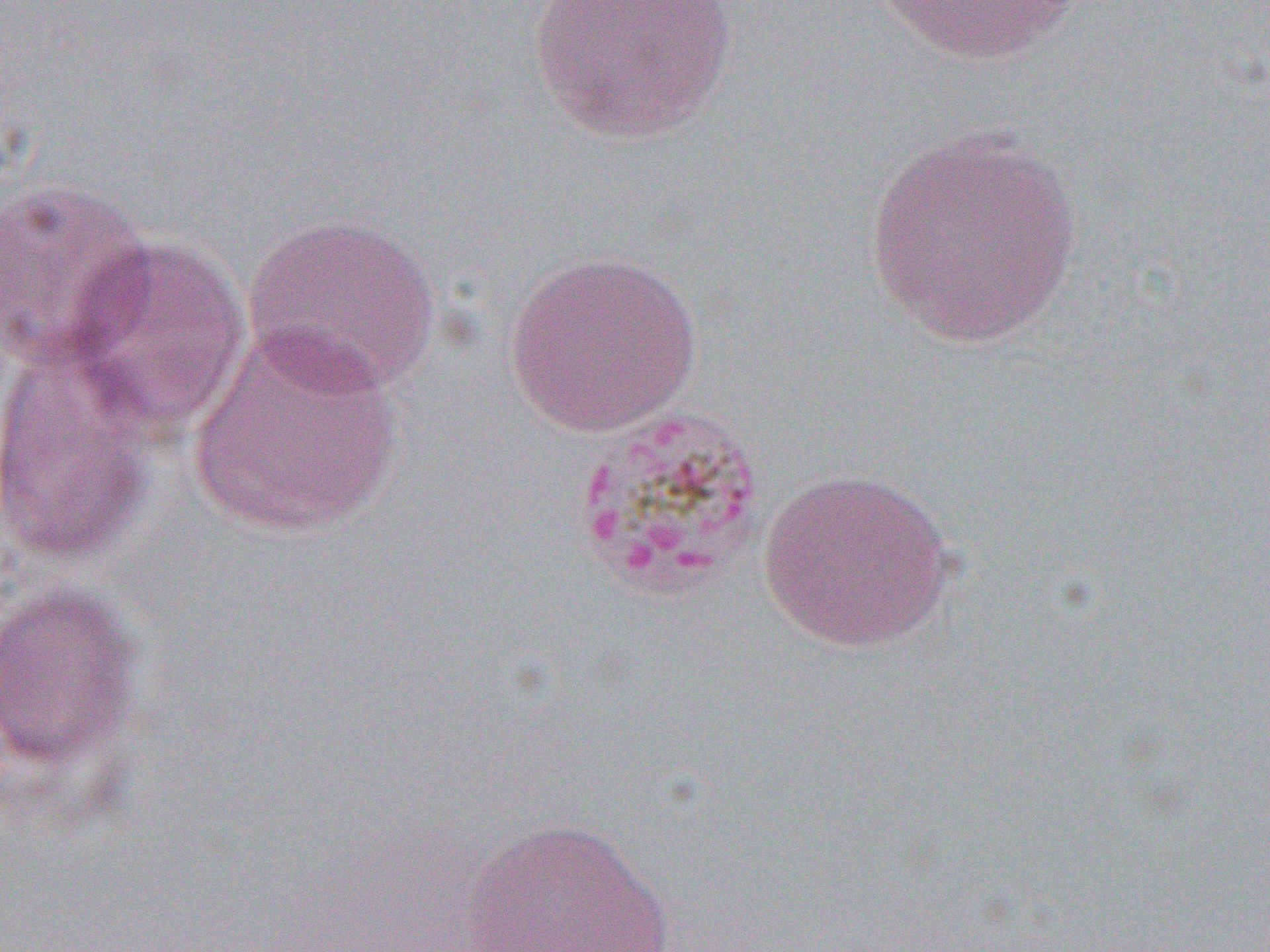
Summary:
  - Coordinate format: approximate bounding boxes as [x1, y1, x2, y2] in pixels
  - Uninfected red blood cell locations: [528, 0, 736, 144], [866, 0, 1089, 66], [865, 124, 1084, 350], [0, 177, 156, 370], [242, 212, 441, 396], [56, 234, 254, 442], [504, 249, 703, 437], [189, 327, 405, 538], [0, 345, 158, 569], [758, 467, 956, 654], [0, 582, 145, 771], [462, 816, 676, 952]
  - Slide-level diagnosis: Plasmodium malariae
  - Preparation: thin blood smear
  - Image size: 1270×952 pixels
  - Magnification: 1000x
  - Field of view: single
  - Modality: optical microscopy